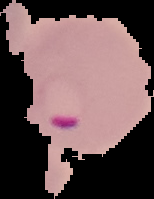
From a thin blood film. Image is 154×199 pixels. Segmented cell region on a black background. Malaria status: parasitized.